Report the malaria status of this cell.
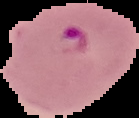
It is parasitized.

image size = 139×118 pixels
image type = cell region segmented out of the field of view; surrounding area masked to black
preparation = thin blood smear